Describe the morphology of the erythrocytes.
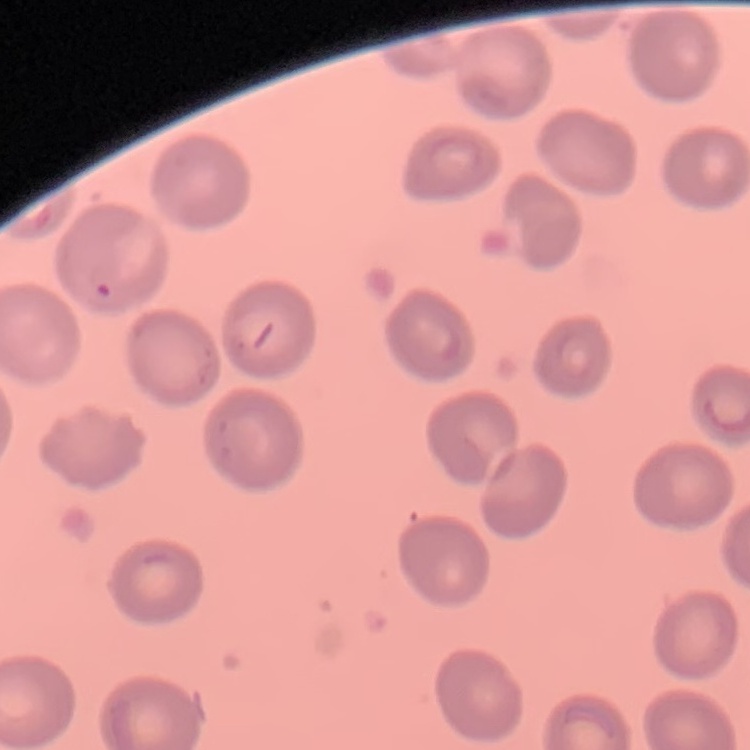

They show no rouleaux formation.

Square crop of a larger photomicrograph. Field's or Giemsa stain. Thin blood film.